Draw a bounding box around every leukocyte (white blood cell).
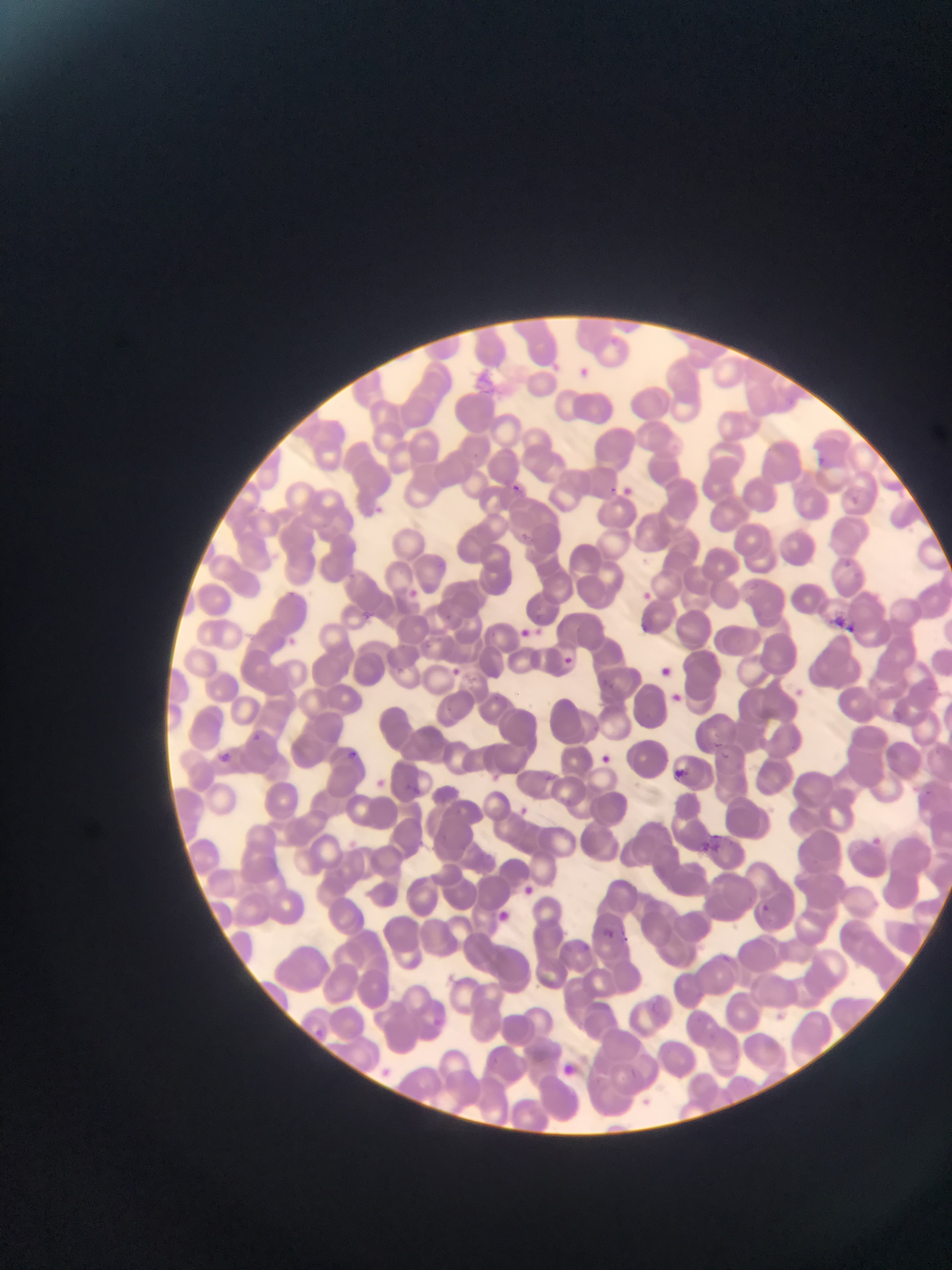
No leukocytes observed.

capture: mobile-phone photograph through a microscope
plasmodium_parasite_locations: 'approximate bounding boxes as [left, top, right, bottom] in pixels: [575, 362, 595, 375], [804, 453, 839, 470], [509, 480, 525, 496], [608, 482, 621, 493], [848, 492, 865, 504], [368, 501, 397, 518], [513, 528, 536, 547], [838, 557, 856, 569], [342, 567, 371, 584], [406, 583, 427, 599], [636, 584, 657, 596], [283, 588, 301, 599], [360, 607, 376, 623], [839, 617, 857, 640], [531, 621, 546, 640], [284, 635, 302, 652], [565, 653, 581, 665], [450, 664, 459, 679], [793, 682, 813, 703], [595, 722, 601, 730], [252, 731, 263, 743], [712, 736, 736, 765], [345, 744, 359, 760], [220, 752, 230, 770], [601, 753, 612, 761], [676, 768, 692, 781], [544, 770, 555, 781], [404, 780, 423, 797], [920, 781, 940, 799], [518, 803, 532, 818], [708, 830, 729, 849], [870, 833, 888, 849], [695, 834, 712, 848], [524, 880, 535, 891], [755, 897, 770, 922], [595, 922, 616, 938], [583, 941, 591, 955]'
preparation: thin blood film
field_of_view: single
country: Ghana
image_size: 952×1270 pixels